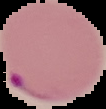
Summary:
  - Image type: segmented cell region on a black background
  - Image size: 106×109 pixels
  - Result: Plasmodium parasites identified
  - Preparation: thin blood smear